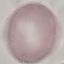
Summary:
  - Malaria status: uninfected
  - Preparation: thin blood smear
  - Stain: Giemsa
  - Image type: automatically extracted cell patch, resized to 64 × 64 pixels
  - Capture: smartphone camera at the microscope eyepiece